Classify this cell by malaria status.
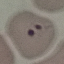

Parasitized.

Summary:
  - Preparation: thin blood film
  - Capture: smartphone through the microscope eyepiece
  - Stain: Giemsa
  - Image type: cell patch, automatically extracted from a larger field of view and resized to 64 × 64 pixels